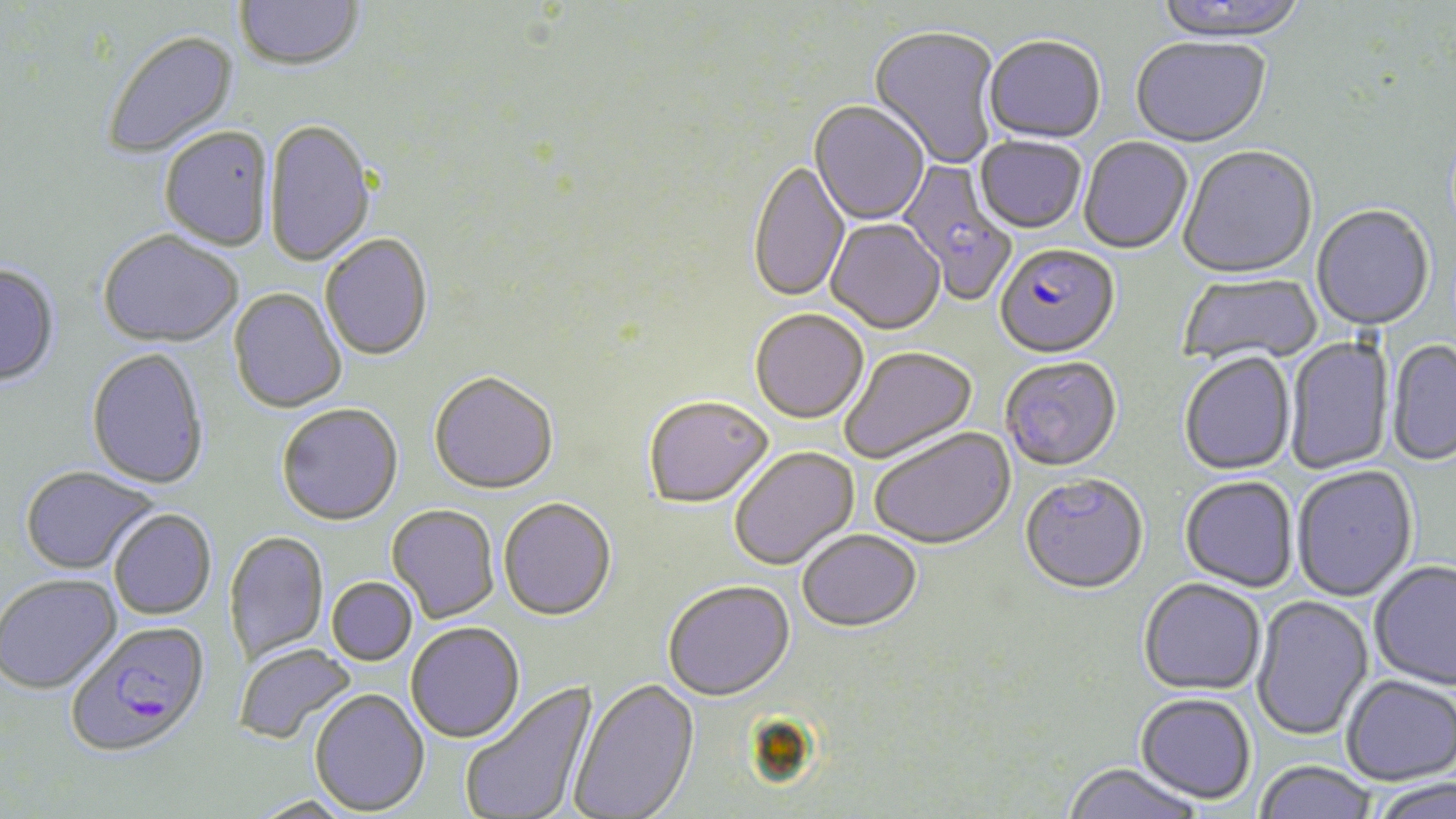

Summary:
  - Coordinate format: approximate bounding boxes as (x1, y1, x2, y2) in pixels
  - Uninfected red blood cell locations: (234, 0, 364, 72), (1151, 0, 1311, 45), (868, 27, 1001, 169), (102, 30, 239, 160), (983, 38, 1106, 146), (1131, 39, 1271, 150), (808, 102, 930, 227), (265, 118, 375, 267), (159, 125, 274, 250), (975, 138, 1086, 236), (1079, 138, 1193, 256), (1178, 147, 1318, 282), (749, 161, 850, 305), (1311, 206, 1435, 333), (826, 220, 946, 337), (97, 229, 243, 347), (320, 234, 433, 361), (0, 264, 60, 386), (1178, 272, 1321, 368), (228, 288, 346, 414), (750, 310, 869, 425), (1284, 335, 1395, 475), (1387, 340, 1456, 467), (840, 347, 977, 466), (86, 348, 210, 489), (1179, 354, 1296, 477), (1000, 359, 1122, 474), (428, 372, 559, 495), (643, 398, 773, 511), (276, 403, 403, 525), (870, 428, 1016, 552), (730, 448, 861, 572), (20, 465, 159, 574), (1292, 467, 1418, 604), (1019, 476, 1149, 598), (1179, 478, 1298, 594), (498, 499, 617, 623), (387, 504, 499, 623), (108, 508, 216, 620), (224, 530, 329, 664), (797, 532, 922, 635), (1369, 562, 1456, 693), (0, 574, 121, 694), (327, 577, 418, 665), (1138, 581, 1266, 697), (662, 582, 795, 704), (1251, 596, 1375, 742), (406, 622, 525, 743), (234, 643, 357, 745), (1341, 676, 1455, 787), (568, 678, 700, 819), (459, 680, 600, 819), (309, 688, 430, 816), (1135, 695, 1256, 806), (1253, 762, 1379, 819), (1061, 765, 1202, 819), (1371, 779, 1455, 819), (248, 796, 357, 818)
  - Plasmodium falciparum-infected red blood cell locations: (896, 155, 1017, 306), (993, 245, 1120, 362), (65, 620, 211, 757)
  - Slide-level diagnosis: Plasmodium falciparum
  - Magnification: 1000x
  - Image size: 1456×819 pixels
  - Preparation: thin blood smear
  - Field of view: single
  - Modality: light microscopy
  - Stain: May-Grünwald-Giemsa